Name the parasite shown.
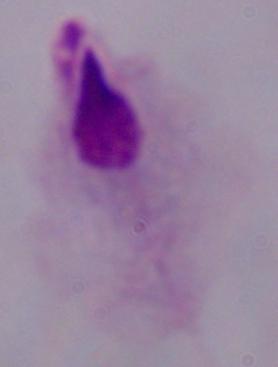

A trichomonad.

Summary:
  - Modality: micrograph
  - Magnification: 1000x